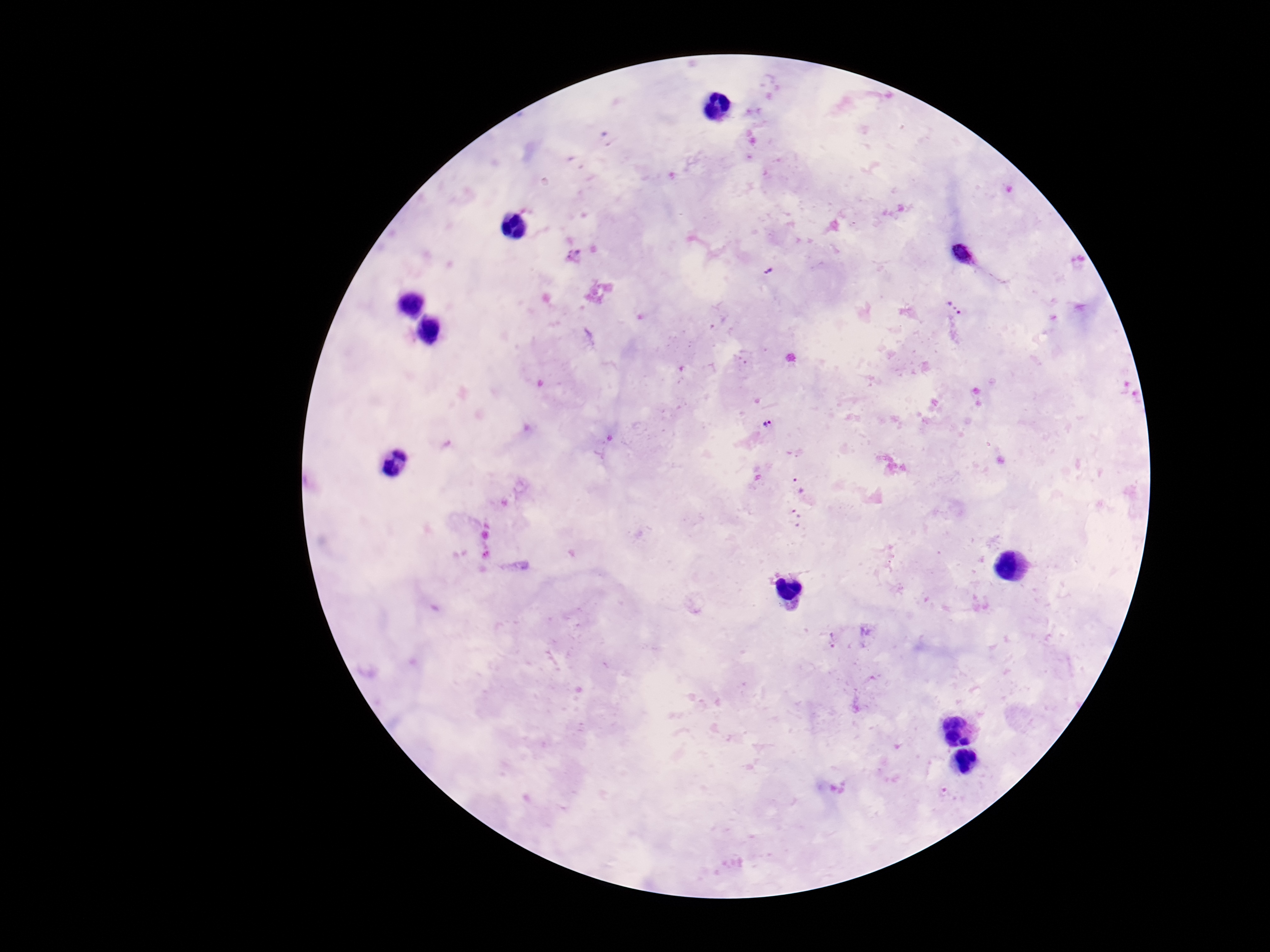
Plasmodium parasite locations = approximate centers as (x, y) in pixels: (954, 308), (769, 424), (798, 486), (795, 518), (832, 639)
preparation = thick peripheral-blood smear
image size = 1270×952 pixels
field of view = one from this slide
stain = Giemsa
magnification = 100x
patient malaria status = infected
capture = smartphone camera through the microscope eyepiece